Report the malaria status of this cell.
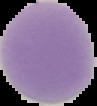
It is uninfected.

The area outside the segmented cell region is set to black. From a thin blood smear. Image is 97×106 pixels.